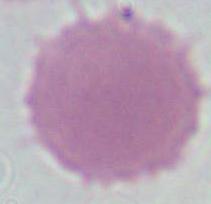

Captured at 1000x magnification. Micrograph. A red blood cell is shown.